Report the malaria status of this cell.
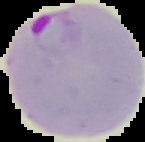
Parasitized.

Summary:
  - Image type: segmented cell region on a black background
  - Preparation: thin blood film
  - Image size: 145×142 pixels